Identify the cell.
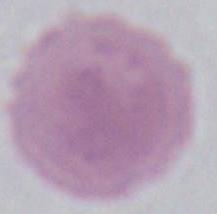
This is an erythrocyte.

Micrograph. Captured at 1000x magnification.